Classify this cell by malaria status.
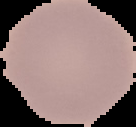
Uninfected.

Summary:
  - Preparation: thin blood smear
  - Image type: segmented cell region on a black background
  - Image size: 136×127 pixels